Outline platelets.
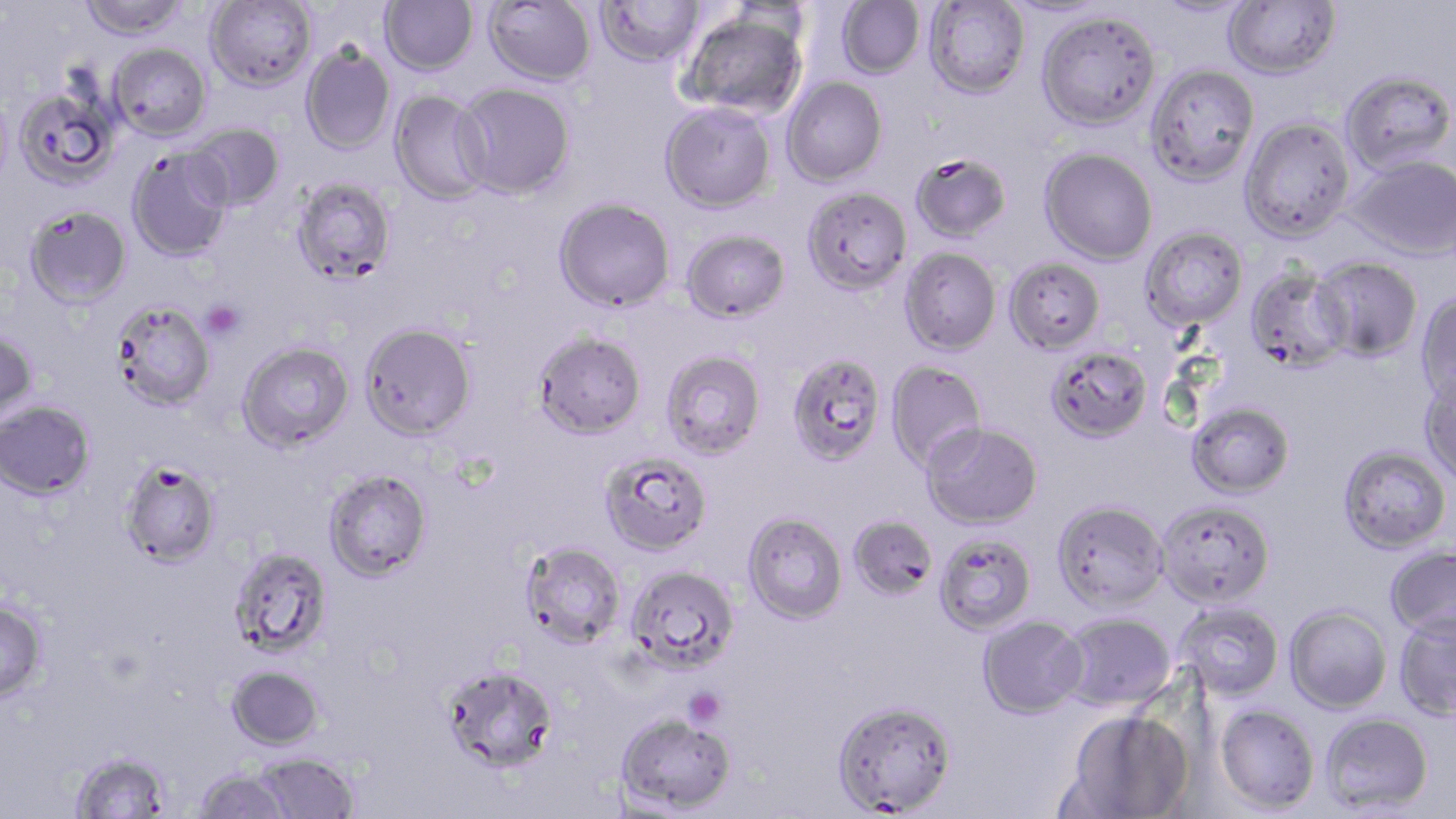

Approximate bounding boxes as (x1,y1)-(x2,y2) corner pairs in pixels.
Platelets: (201,300)-(245,340), (684,687)-(726,729).

Uninfected red blood cell locations: (77,0)-(191,42), (205,0)-(317,92), (380,0)-(477,76), (484,0)-(596,87), (595,0)-(706,67), (1223,0)-(1341,80), (835,1)-(925,80), (923,1)-(1030,99), (1001,1)-(1121,20), (1150,1)-(1259,20), (680,9)-(809,120), (1035,10)-(1161,131), (108,43)-(212,141), (300,45)-(395,155), (1144,63)-(1260,186), (1340,69)-(1455,175), (781,76)-(887,186), (454,83)-(575,199), (12,85)-(119,191), (389,90)-(494,206), (0,92)-(14,198), (660,101)-(777,214), (1239,116)-(1356,242), (188,123)-(284,212), (1039,147)-(1158,265), (126,149)-(233,263), (910,152)-(1013,244), (1347,154)-(1456,261), (291,176)-(396,287), (802,186)-(913,295), (554,197)-(675,313), (24,205)-(132,311), (1140,226)-(1249,331), (682,229)-(791,323), (899,247)-(1002,356), (1311,256)-(1423,361), (1004,257)-(1106,355), (1245,266)-(1351,372), (1415,291)-(1456,407), (112,302)-(215,413), (360,323)-(476,442), (0,331)-(39,426), (532,331)-(646,441), (237,342)-(354,453), (1046,346)-(1154,444), (661,350)-(766,460), (786,353)-(887,467), (885,361)-(988,470), (1419,375)-(1456,487), (0,402)-(96,501), (1187,402)-(1295,498), (921,421)-(1043,529), (1338,444)-(1452,553), (600,452)-(713,556), (120,459)-(220,569), (323,468)-(432,582), (1051,499)-(1168,612), (1156,499)-(1275,608), (743,511)-(848,624), (847,514)-(938,601), (934,533)-(1037,635), (520,541)-(625,649), (1385,545)-(1456,639), (229,546)-(333,657), (625,565)-(739,674), (0,599)-(49,704), (1174,602)-(1285,701), (1285,605)-(1392,714), (1393,611)-(1456,721), (1059,612)-(1177,711), (977,614)-(1088,719), (441,664)-(558,775), (227,665)-(324,751), (832,698)-(957,816), (1215,704)-(1321,813), (1064,710)-(1193,819), (616,712)-(737,814), (1321,712)-(1434,814), (70,752)-(171,818), (254,752)-(359,818), (192,768)-(294,819). Slide-level diagnosis: Plasmodium falciparum. Single field of view. Thin blood film. Light microscopy. Image is 1456×819 pixels. 1000x magnification. May-Grünwald-Giemsa-stained preparation.